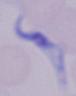
modality: photomicrograph
magnification: 1000x
identification: trypanosome